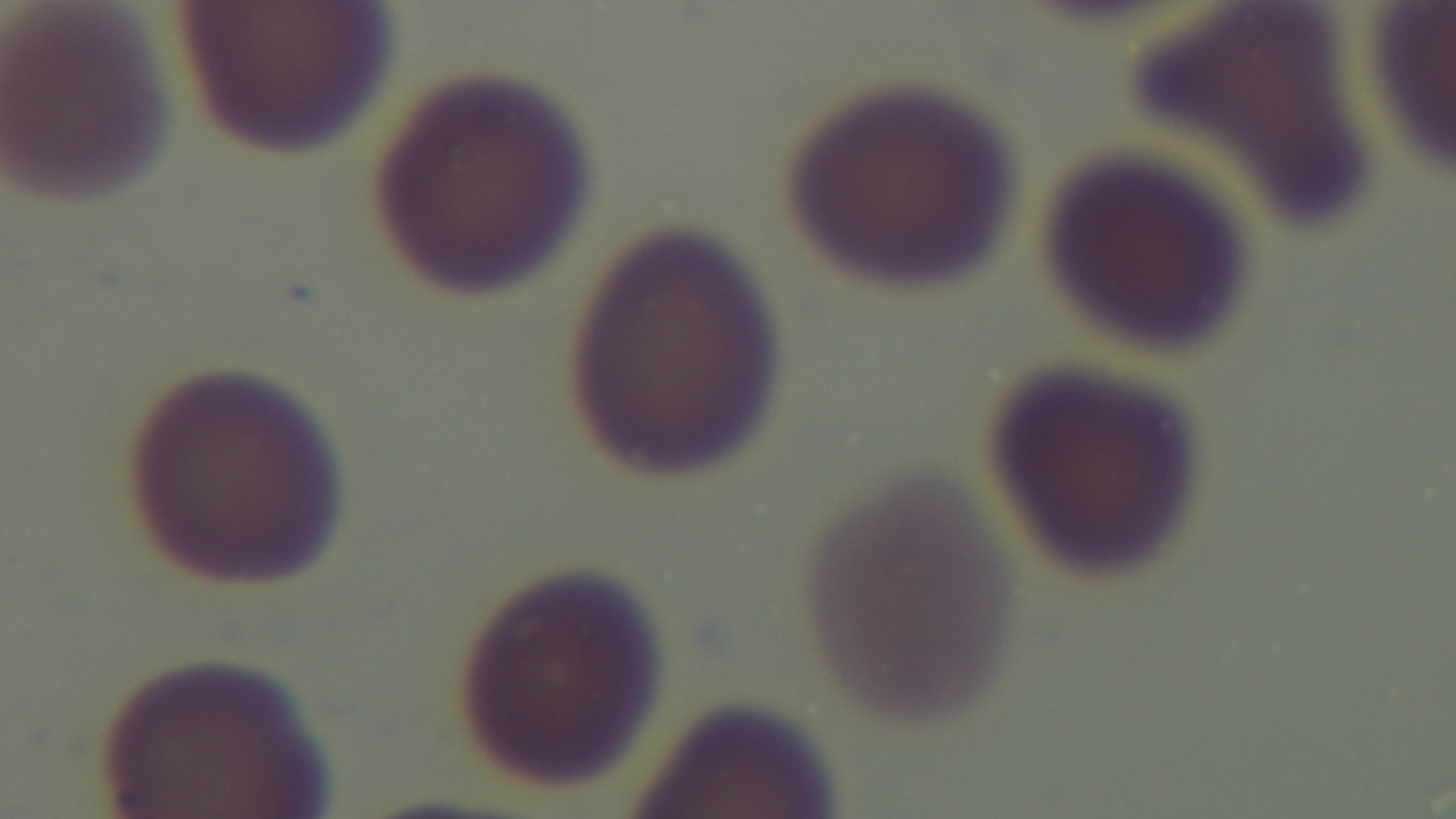
Summary:
  - Capture: mounted 4K digital camera
  - Preparation: thin
  - Field of view: one from the slide
  - Modality: light microscopy
  - Malaria status: negative
  - Objective: 100x oil immersion
  - Stain: Giemsa